Give the position of every Plasmodium parasite visible.
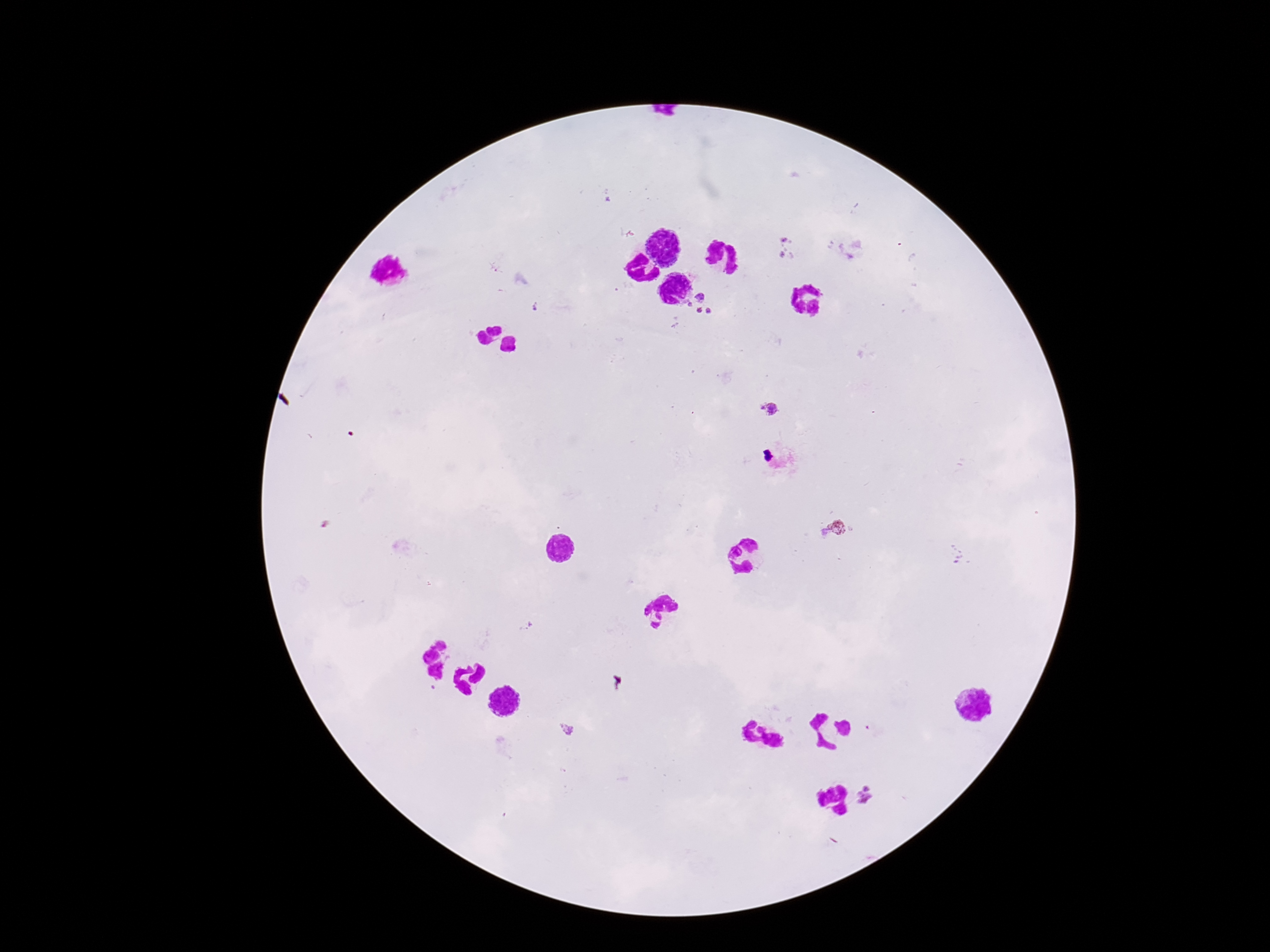

Approximate centers as [x, y] in pixels.
Plasmodium parasites: [787, 239], [786, 256], [493, 268], [699, 295], [689, 304], [698, 309], [708, 312], [769, 410], [835, 529], [566, 728], [869, 796].

Summary:
  - Stain: Giemsa
  - Preparation: thick blood film
  - Magnification: 100x
  - Capture: smartphone camera through the microscope eyepiece
  - Patient malaria status: positive
  - Image size: 1270×952 pixels
  - Field of view: one from this slide